Describe the morphology of the red blood cells.
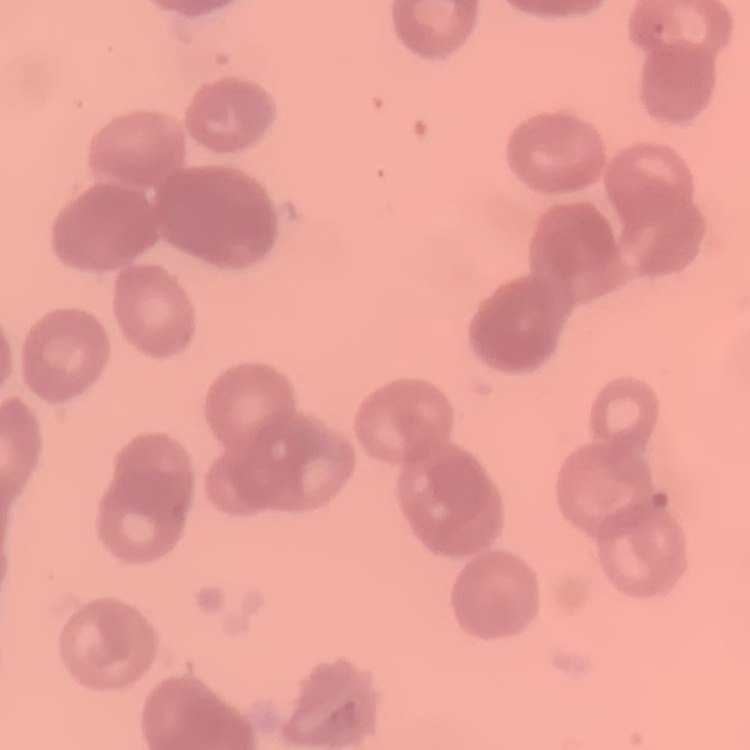

They show rouleaux formation.

Summary:
  - Stain: Field's or Giemsa
  - Image type: one tile cut from a larger photomicrograph
  - Preparation: thin peripheral smear